State which parasite is depicted.
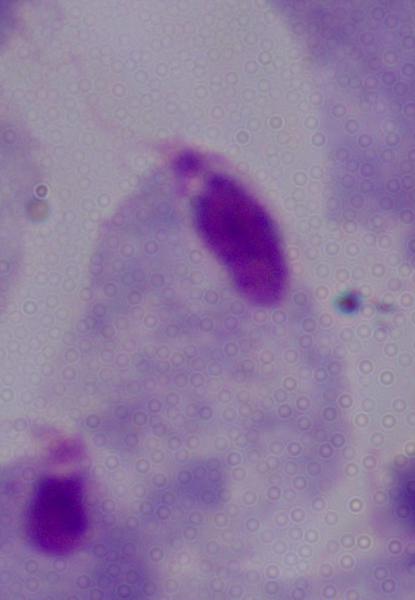
This is a trichomonad.

Photomicrograph. Captured at 1000x magnification.